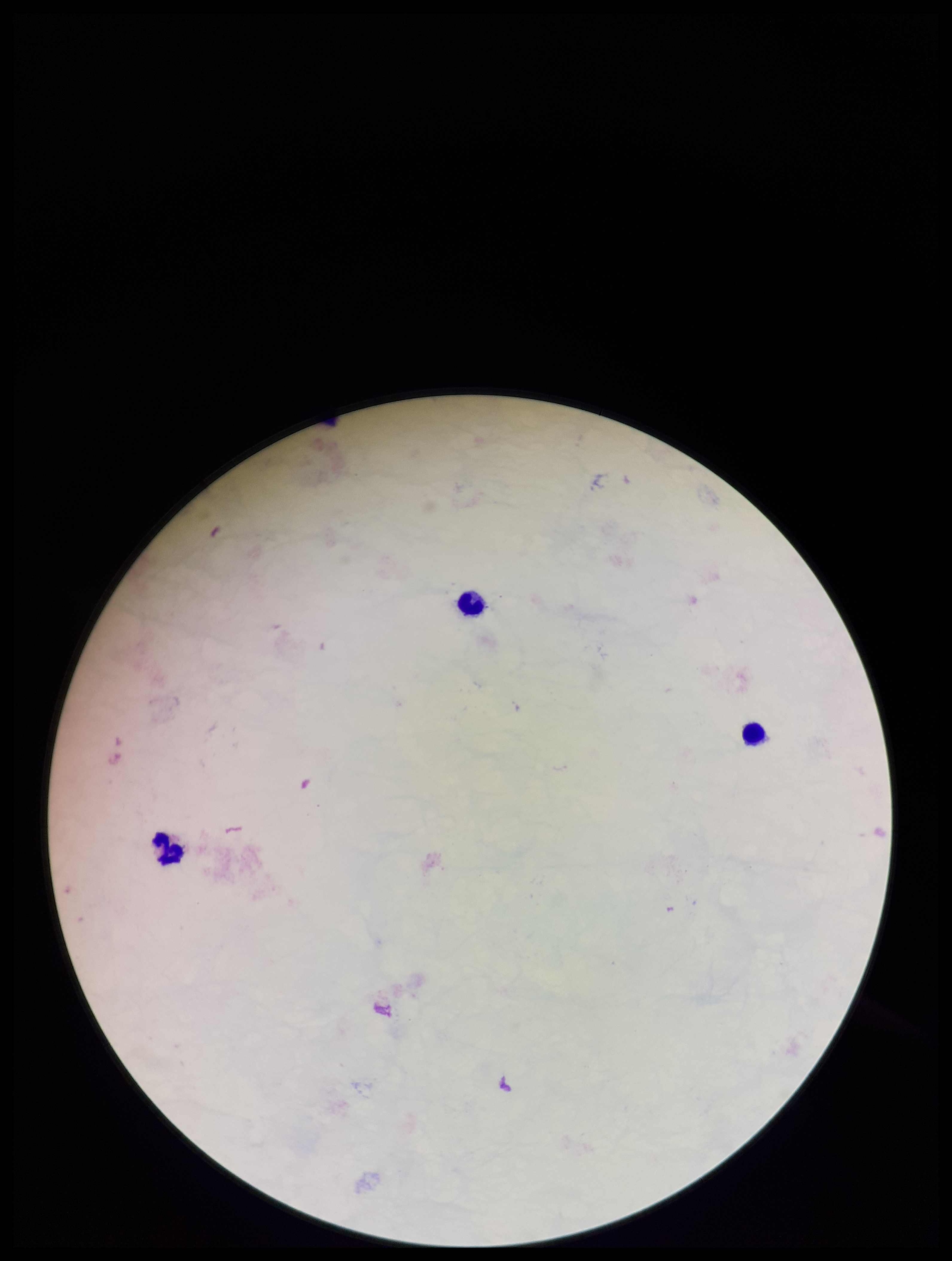

Image is 952×1261 pixels. Preparation: thick blood smear. Smartphone photograph taken through the eyepiece of a microscope. Leukocyte count: 3. Parasite count: 0. Patient malaria status: negative. Giemsa stain. Plasmodium parasites: none detected. Single field of view.